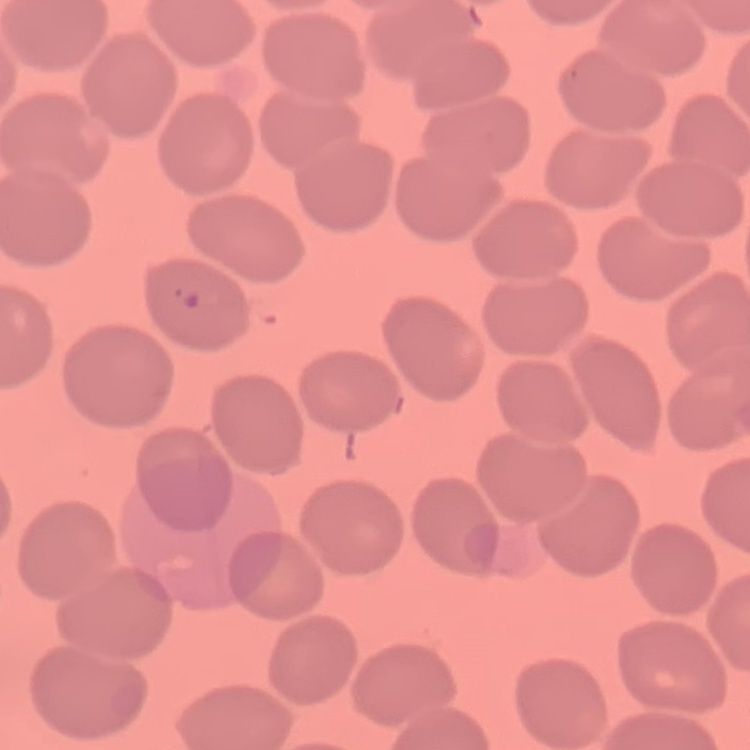

Summary:
  - Erythrocyte morphology: no rouleaux formation
  - Preparation: thin blood film
  - Stain: Field's or Giemsa
  - Image type: square crop of a larger photomicrograph